Name the parasite shown.
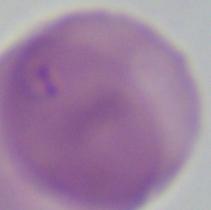
Babesia.

Summary:
  - Modality: photomicrograph
  - Magnification: 1000x